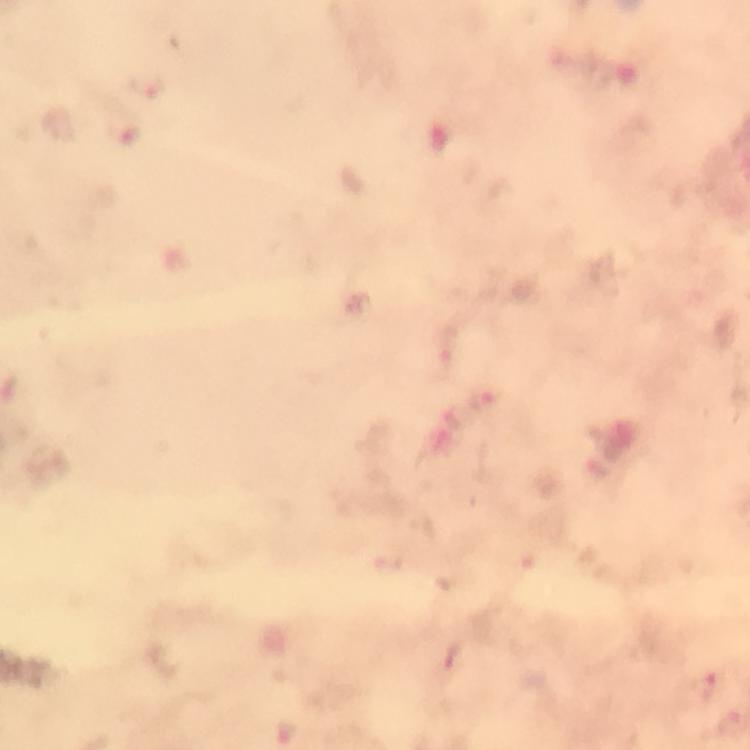
cropped from = a single field of view
preparation = thick smear
stain = Giemsa
magnification = 100x
image size = 750×750 pixels
immersion oil = used
Plasmodium parasite locations = approximate centers as [x, y] in pixels: [447, 344], [482, 400], [711, 684], [730, 720]
capture = smartphone camera through the microscope
context = from a diagnostic examination for malaria